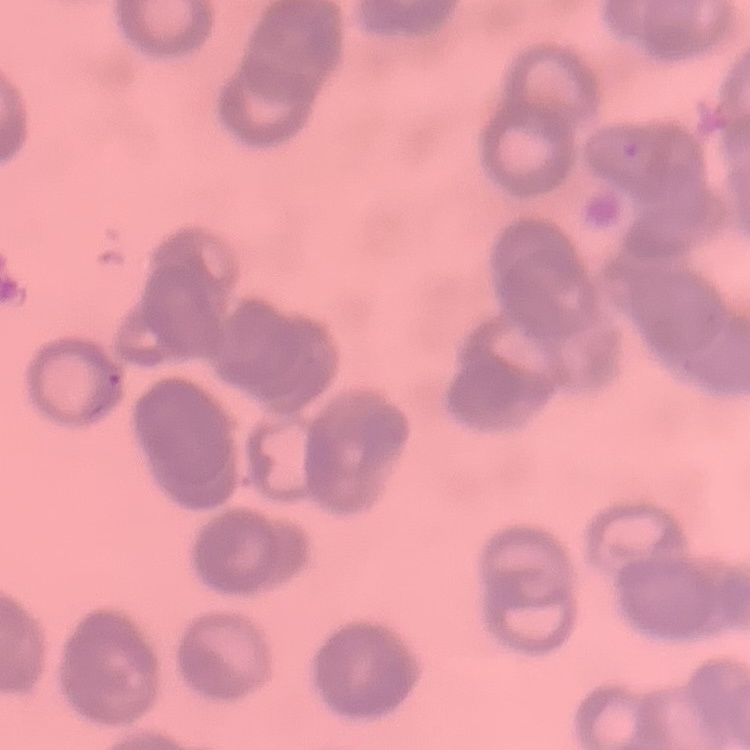

Summary:
  - Red blood cell morphology: rouleaux formation
  - Preparation: thin blood smear
  - Image type: one tile cut from a larger photomicrograph
  - Stain: Field's or Giemsa